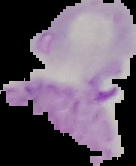
From a thin blood film. The area outside the segmented cell region is set to black. Result: Plasmodium parasites identified. Image is 136×166 pixels.